Classify this cell by malaria status.
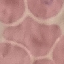

It is uninfected.

Thin blood smear. Acquired by smartphone through the microscope eyepiece. Giemsa stain. Automatically extracted cell patch, resized to 64 × 64 pixels.